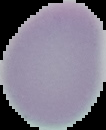
malaria status = uninfected
image type = segmented cell region with the area outside set to black
image size = 106×130 pixels
preparation = thin blood film